Name the blood parasite species.
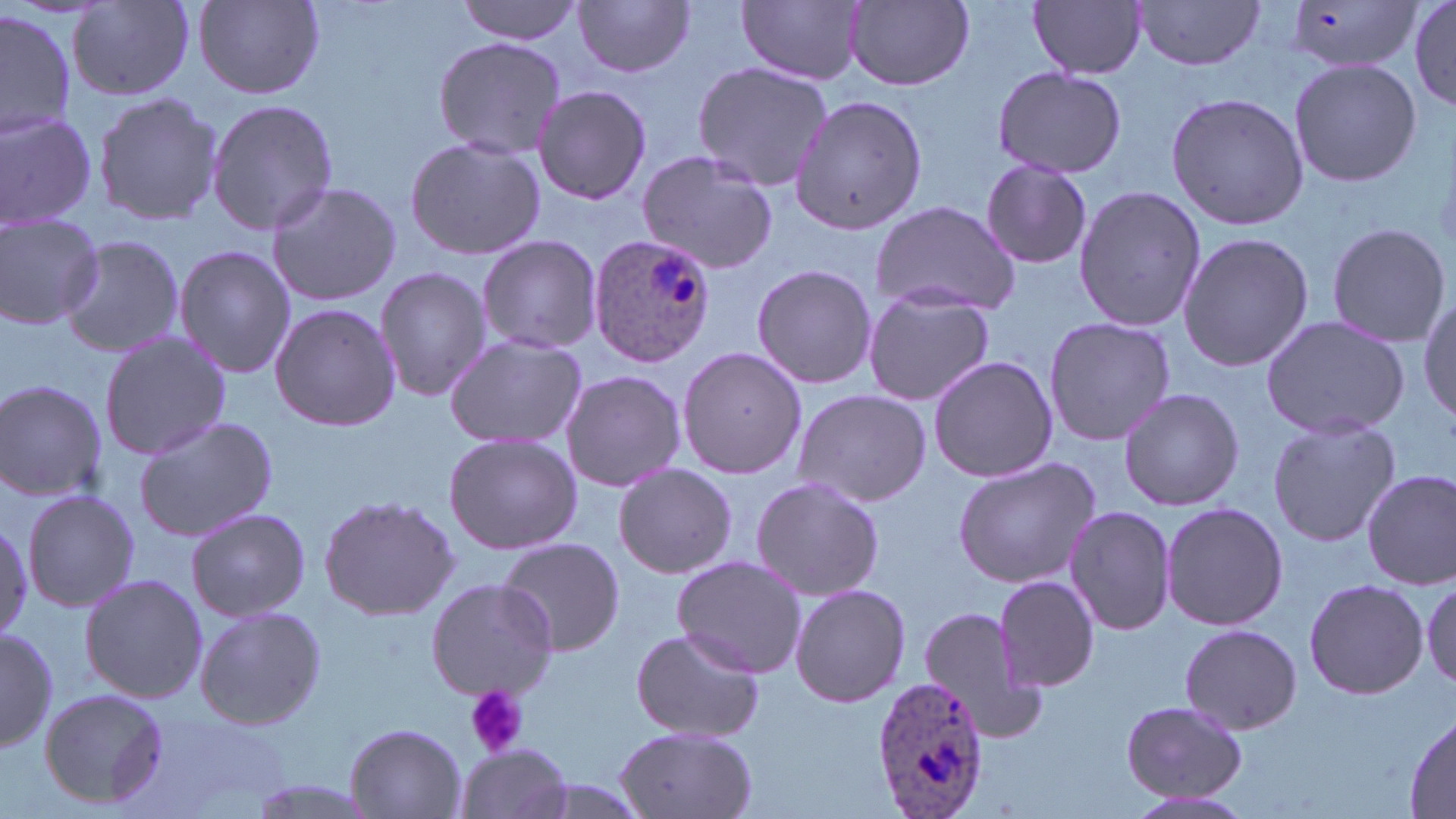

Plasmodium ovale.

Approximate bounding boxes as (x1, y1, x2, y2) in pixels. Uninfected red blood cell locations: (191, 0, 329, 101), (459, 0, 584, 45), (739, 0, 865, 85), (1409, 0, 1456, 113), (574, 1, 696, 79), (843, 1, 975, 93), (1028, 1, 1147, 79), (1132, 1, 1264, 70), (1285, 1, 1425, 74), (70, 3, 194, 100), (0, 11, 75, 140), (432, 35, 567, 160), (1288, 57, 1422, 189), (691, 61, 835, 191), (992, 65, 1129, 180), (533, 85, 653, 207), (1165, 90, 1310, 230), (92, 91, 224, 228), (790, 95, 927, 233), (206, 97, 338, 236), (0, 110, 100, 231), (405, 136, 546, 263), (636, 151, 778, 274), (980, 159, 1094, 270), (265, 179, 402, 307), (1071, 186, 1208, 332), (870, 199, 1023, 318), (0, 215, 106, 330), (1326, 222, 1451, 348), (1177, 231, 1315, 371), (474, 234, 602, 355), (57, 235, 187, 357), (174, 244, 296, 379), (752, 263, 878, 390), (374, 267, 490, 401), (862, 286, 995, 408), (1420, 296, 1456, 424), (269, 303, 403, 431), (1260, 314, 1410, 440), (1043, 316, 1175, 448), (99, 329, 230, 463), (444, 335, 588, 450), (675, 345, 807, 481), (927, 355, 1059, 482), (559, 369, 687, 494), (0, 378, 108, 502), (790, 387, 932, 508), (1118, 387, 1243, 511), (1267, 415, 1400, 547), (134, 416, 278, 543), (444, 432, 582, 555), (952, 455, 1100, 587), (613, 463, 737, 579), (1362, 470, 1455, 590), (750, 476, 883, 602), (21, 489, 141, 611), (318, 493, 461, 623), (1162, 501, 1289, 631), (1063, 504, 1175, 637), (185, 506, 312, 622), (0, 513, 32, 642), (493, 536, 626, 656), (672, 554, 808, 679), (79, 572, 208, 704), (992, 574, 1101, 693), (1303, 576, 1428, 702), (424, 577, 558, 701), (1420, 577, 1455, 693), (788, 582, 911, 708), (916, 604, 1051, 745), (194, 605, 328, 730), (1179, 623, 1303, 736), (0, 626, 58, 753), (629, 626, 766, 743), (39, 686, 170, 811), (1119, 699, 1248, 804), (1406, 714, 1455, 815), (343, 723, 468, 818), (613, 725, 759, 819), (453, 744, 576, 819), (237, 776, 387, 819), (1120, 790, 1261, 819). Plasmodium ovale-infected red blood cell locations: (584, 231, 719, 366), (870, 677, 991, 816). Platelet locations: (463, 685, 528, 757). One field of a larger specimen. Image is 1456×819 pixels. Light microscopy. Thin blood film. 1000x magnification. May-Grünwald-Giemsa stain.